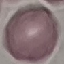

{
  "result": "negative for malaria parasites",
  "capture": "smartphone camera at the microscope eyepiece",
  "preparation": "thin blood film",
  "stain": "Giemsa",
  "image_type": "cell patch, automatically extracted from a larger field of view and resized to 64 × 64 pixels"
}